Locate every Plasmodium parasite.
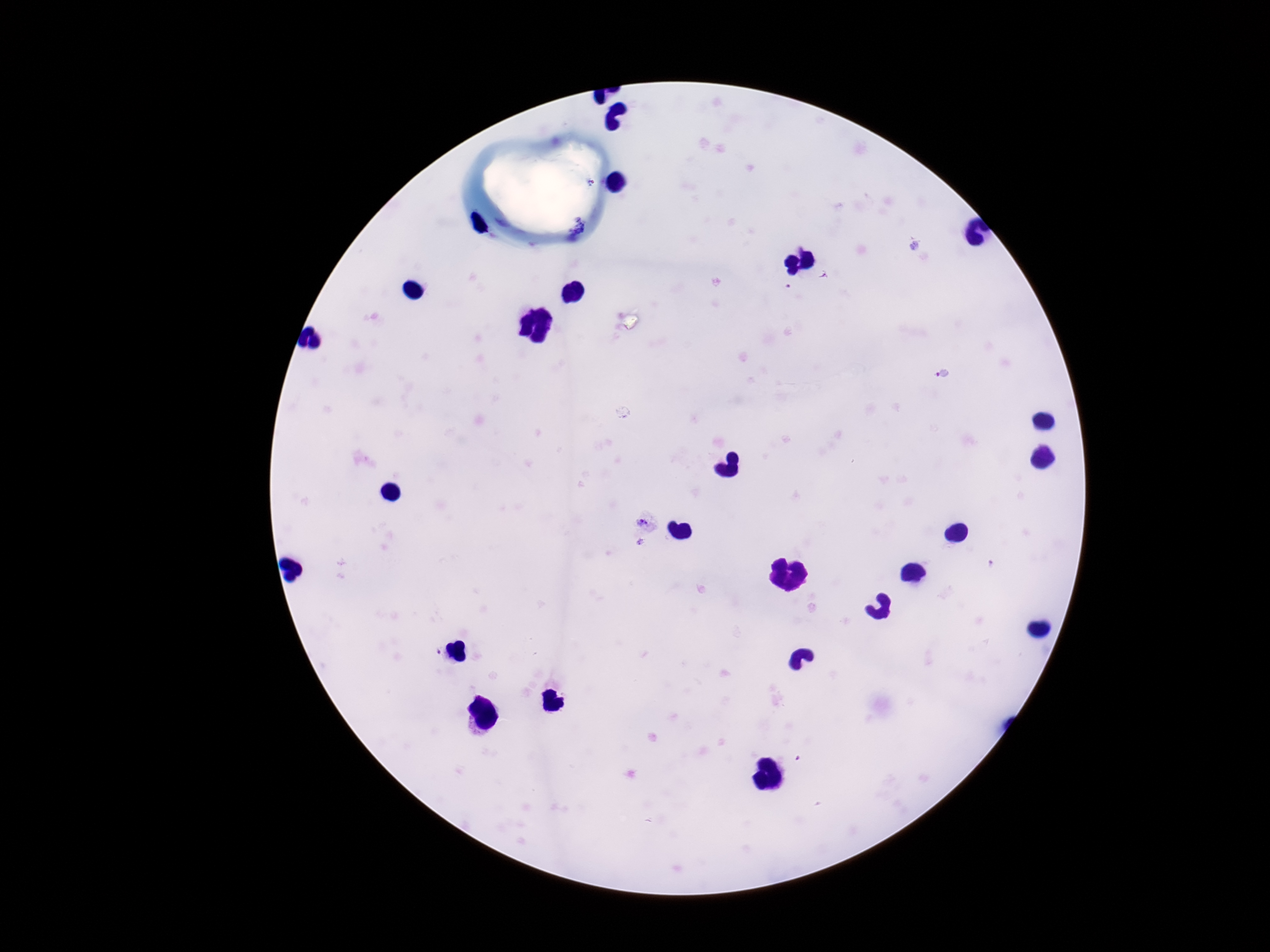

Approximate object centers, in pixels from the top-left corner.
Plasmodium parasites: (x=944, y=373), (x=644, y=523), (x=437, y=652).

magnification = 100x
stain = Giemsa
capture = smartphone camera through the microscope eyepiece
field of view = one from this slide
image size = 1270×952 pixels
patient malaria status = positive
preparation = thick blood smear